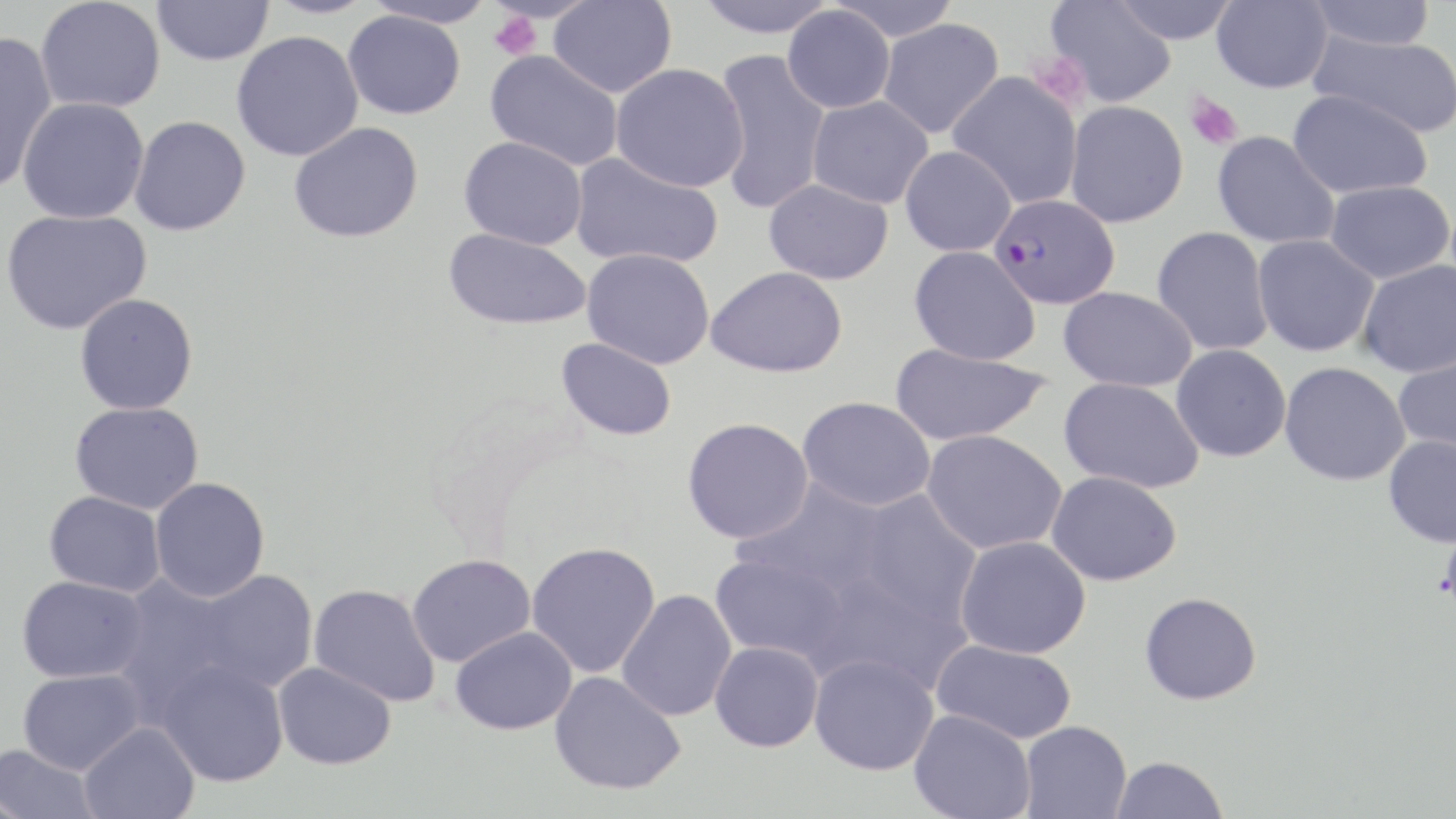
slide-level diagnosis = Plasmodium falciparum
platelet locations = approximate bounding boxes as (x1,y1)-(x2,y2) corner pairs in pixels: (488,11)-(541,60), (1027,50)-(1089,109), (1184,91)-(1244,151)
Plasmodium falciparum-infected red blood cell locations = approximate bounding boxes as (x1,y1)-(x2,y2) corner pairs in pixels: (989,194)-(1120,309)
magnification = 1000x
uninfected red blood cell locations = approximate bounding boxes as (x1,y1)-(x2,y2) corner pairs in pixels: (152,0)-(274,66), (263,0)-(377,19), (361,0)-(497,29), (548,0)-(677,98), (693,0)-(836,38), (825,0)-(961,41), (1211,0)-(1333,94), (1306,0)-(1438,51), (36,1)-(165,113), (1045,1)-(1178,107), (1111,1)-(1240,44), (782,6)-(896,114), (343,10)-(466,120), (877,18)-(1004,138), (0,30)-(58,193), (230,30)-(364,162), (1309,31)-(1456,139), (712,49)-(832,215), (485,50)-(623,171), (610,63)-(749,191), (947,71)-(1083,208), (1287,89)-(1433,199), (807,95)-(934,209), (17,97)-(150,225), (1065,100)-(1189,227), (128,115)-(250,236), (289,121)-(424,243), (1211,131)-(1341,250), (458,136)-(588,250), (899,145)-(1017,257), (570,152)-(724,270), (764,178)-(894,285), (1324,181)-(1454,284), (0,208)-(152,335), (1151,226)-(1274,356), (443,228)-(592,330), (1251,234)-(1380,357), (909,246)-(1041,366), (582,248)-(715,369), (1357,259)-(1456,378), (707,265)-(848,378), (1058,286)-(1198,392), (74,293)-(198,415), (556,337)-(677,441), (889,343)-(1051,446), (1171,344)-(1291,462), (1393,351)-(1456,459), (1279,362)-(1411,486), (1058,376)-(1205,493), (798,396)-(936,512), (69,402)-(204,514), (682,417)-(814,543), (921,430)-(1067,555), (1382,434)-(1456,548), (1045,470)-(1182,587), (149,477)-(270,602), (733,480)-(889,597), (848,490)-(983,628), (44,491)-(166,597), (954,536)-(1092,659), (526,541)-(661,678), (710,553)-(849,664), (406,554)-(535,667), (186,569)-(319,696), (112,573)-(245,721), (16,575)-(148,683), (308,583)-(440,707), (616,589)-(737,721), (1139,591)-(1262,705), (449,625)-(577,735), (931,640)-(1077,744), (709,641)-(824,752), (809,653)-(939,776), (157,659)-(288,787), (273,662)-(396,770), (17,668)-(145,775), (549,670)-(686,795), (909,710)-(1036,819), (1019,721)-(1131,818), (79,722)-(200,819), (0,743)-(100,819), (1109,755)-(1229,818)
modality = light microscopy
image size = 1456×819 pixels
field of view = single
stain = May-Grünwald-Giemsa
preparation = thin blood smear